Give the position of every leukocyte visible.
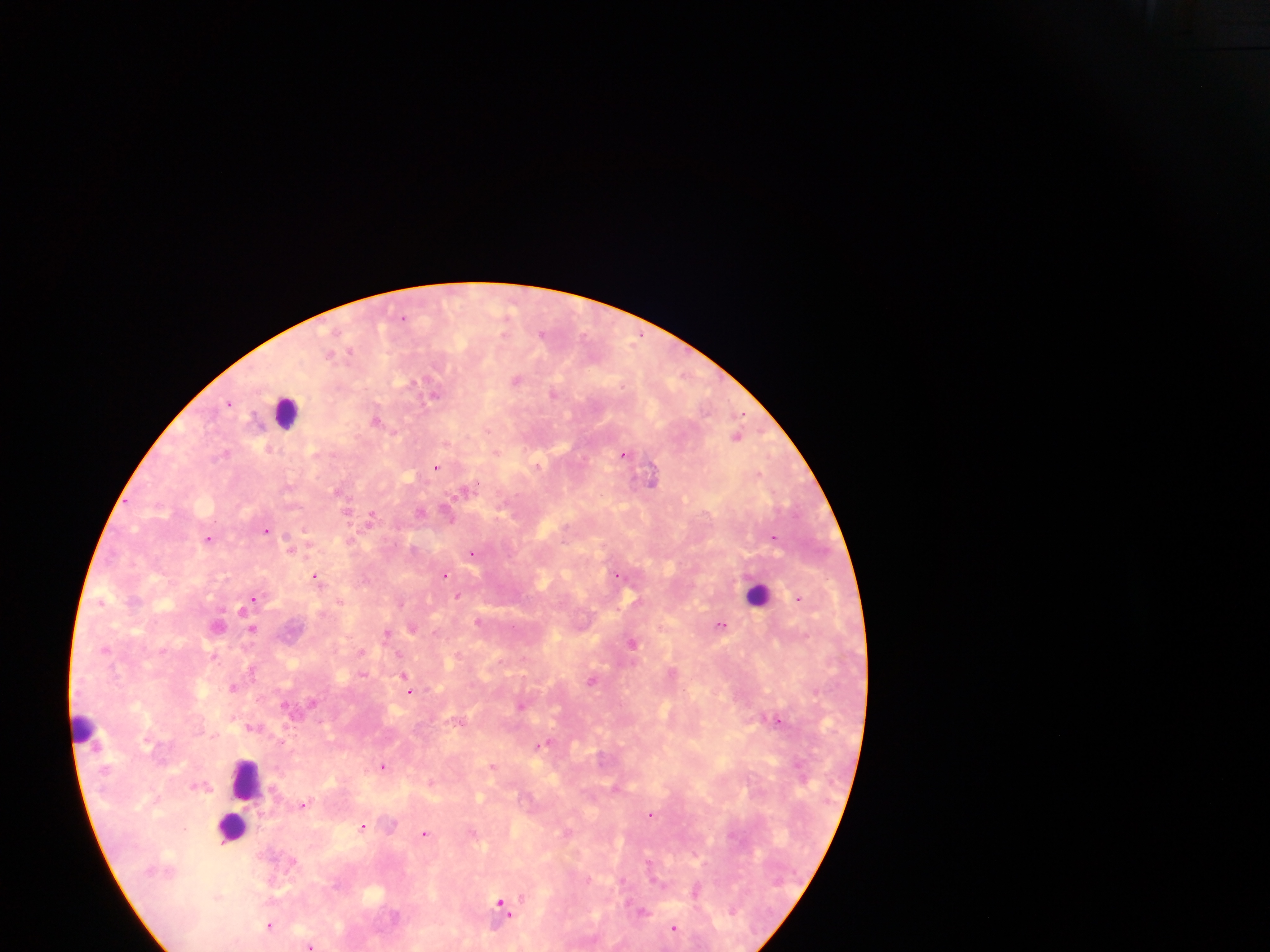
Approximate centers as {x, y} in pixels.
Leukocytes: {287, 412}, {758, 593}, {80, 732}, {246, 779}, {230, 827}.

Summary:
  - Plasmodium parasite locations: {508, 312}, {403, 318}, {542, 333}, {350, 351}, {330, 354}, {516, 379}, {411, 382}, {554, 394}, {434, 396}, {230, 403}, {376, 420}, {737, 435}, {496, 453}, {224, 454}, {625, 455}, {436, 467}, {652, 479}, {466, 489}, {339, 491}, {421, 512}, {371, 517}, {450, 519}, {267, 530}, {773, 537}, {208, 538}, {290, 548}, {473, 553}, {618, 574}, {444, 576}, {317, 578}, {458, 596}, {800, 597}, {253, 598}, {101, 601}, {340, 602}, {401, 603}, {249, 604}, {244, 609}, {477, 621}, {218, 624}, {722, 625}, {253, 630}, {387, 633}, {632, 643}, {105, 649}, {214, 655}, {253, 672}, {363, 674}, {404, 677}, {593, 680}, {233, 686}, {409, 692}, {520, 705}, {779, 720}, {542, 745}, {493, 765}, {383, 766}, {430, 781}, {303, 805}, {651, 814}, {363, 826}, {425, 833}, {696, 890}, {502, 903}, {643, 911}, {269, 924}, {674, 927}, {310, 945}
  - Field of view: single
  - Preparation: thick blood film
  - Country: Ghana
  - Image size: 1270×952 pixels
  - Capture: mobile-phone photograph through a microscope